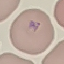

malaria status = parasitized
preparation = thin smear
image type = automatically extracted cell patch, resized to 64 × 64 pixels
stain = Giemsa
capture = smartphone camera at the microscope eyepiece